Assess the morphology of the erythrocytes.
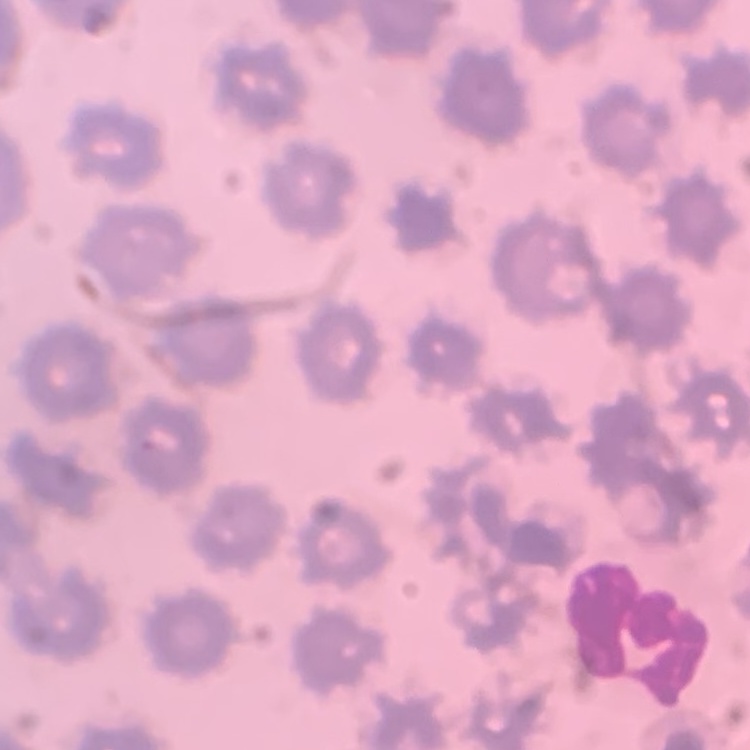
No rouleaux formation.

Field's or Giemsa stain. One tile cut from a larger photomicrograph. Thin blood smear.